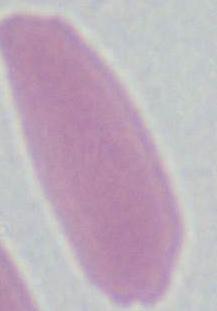
Summary:
  - Modality: micrograph
  - Magnification: 1000x
  - Identification: erythrocyte